Outline each blood parasite and name the species.
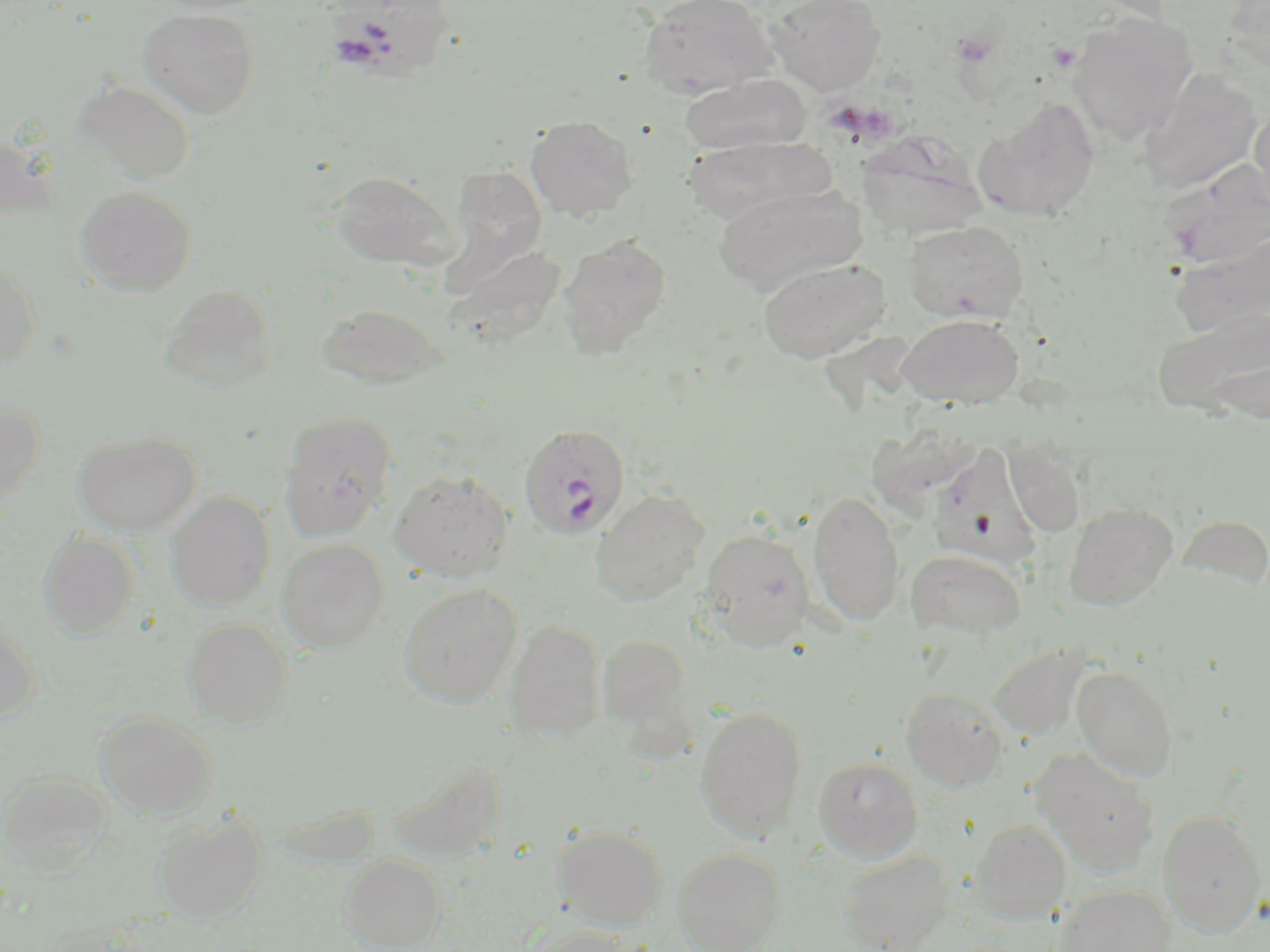
Approximate bounding boxes as (x1,y1)-(x2,y2) corner pairs in pixels.
Plasmodium falciparum-infected red blood cells: (518,423)-(629,539).
No Plasmodium ovale, Plasmodium malariae, Plasmodium vivax, Babesia divergens, or Trypanosoma brucei observed.

Summary:
  - Uninfected red blood cell locations: (325,0)-(459,83), (638,0)-(779,98), (766,0)-(886,94), (1223,0)-(1270,72), (138,8)-(259,118), (1067,12)-(1198,144), (1138,67)-(1263,195), (680,74)-(810,156), (72,81)-(196,185), (973,98)-(1101,223), (1248,103)-(1270,214), (525,116)-(638,220), (859,134)-(987,242), (684,136)-(832,226), (0,137)-(62,223), (1160,159)-(1270,274), (447,168)-(548,276), (329,171)-(456,269), (714,184)-(866,295), (75,186)-(196,296), (904,220)-(1029,323), (1168,230)-(1270,340), (558,234)-(671,358), (448,246)-(566,348), (757,257)-(890,363), (0,262)-(41,369), (157,285)-(276,394), (317,304)-(448,390), (1153,306)-(1270,420), (897,314)-(1025,408), (0,401)-(43,509), (278,412)-(397,540), (73,432)-(202,534), (1003,439)-(1086,536), (930,444)-(1044,563), (388,471)-(514,582), (591,488)-(711,606), (808,491)-(905,628), (166,492)-(275,610), (1064,502)-(1178,609), (1177,513)-(1270,590), (699,529)-(815,649), (38,532)-(139,639), (277,540)-(389,652), (906,549)-(1026,640), (398,585)-(521,707), (182,618)-(292,727), (505,620)-(606,742), (0,622)-(40,723), (597,633)-(694,740), (989,644)-(1088,738), (1072,665)-(1178,781), (900,688)-(1009,790), (695,707)-(807,841), (96,712)-(217,820), (1030,748)-(1160,874), (813,756)-(923,862), (1,771)-(112,874), (154,811)-(268,923), (1157,811)-(1266,934), (971,819)-(1072,923), (553,825)-(668,930), (673,848)-(785,952), (839,851)-(954,952), (340,856)-(446,950), (1053,885)-(1175,952), (524,927)-(641,952)
  - Platelet locations: (1048,43)-(1081,72)
  - Slide-level diagnosis: Plasmodium falciparum
  - Stain: May-Grünwald-Giemsa
  - Field of view: one of a larger specimen
  - Preparation: thin blood film
  - Magnification: 1000x
  - Image size: 1270×952 pixels
  - Modality: optical microscopy